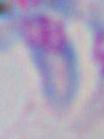
Summary:
  - Modality: micrograph
  - Identification: Toxoplasma gondii
  - Magnification: 1000x